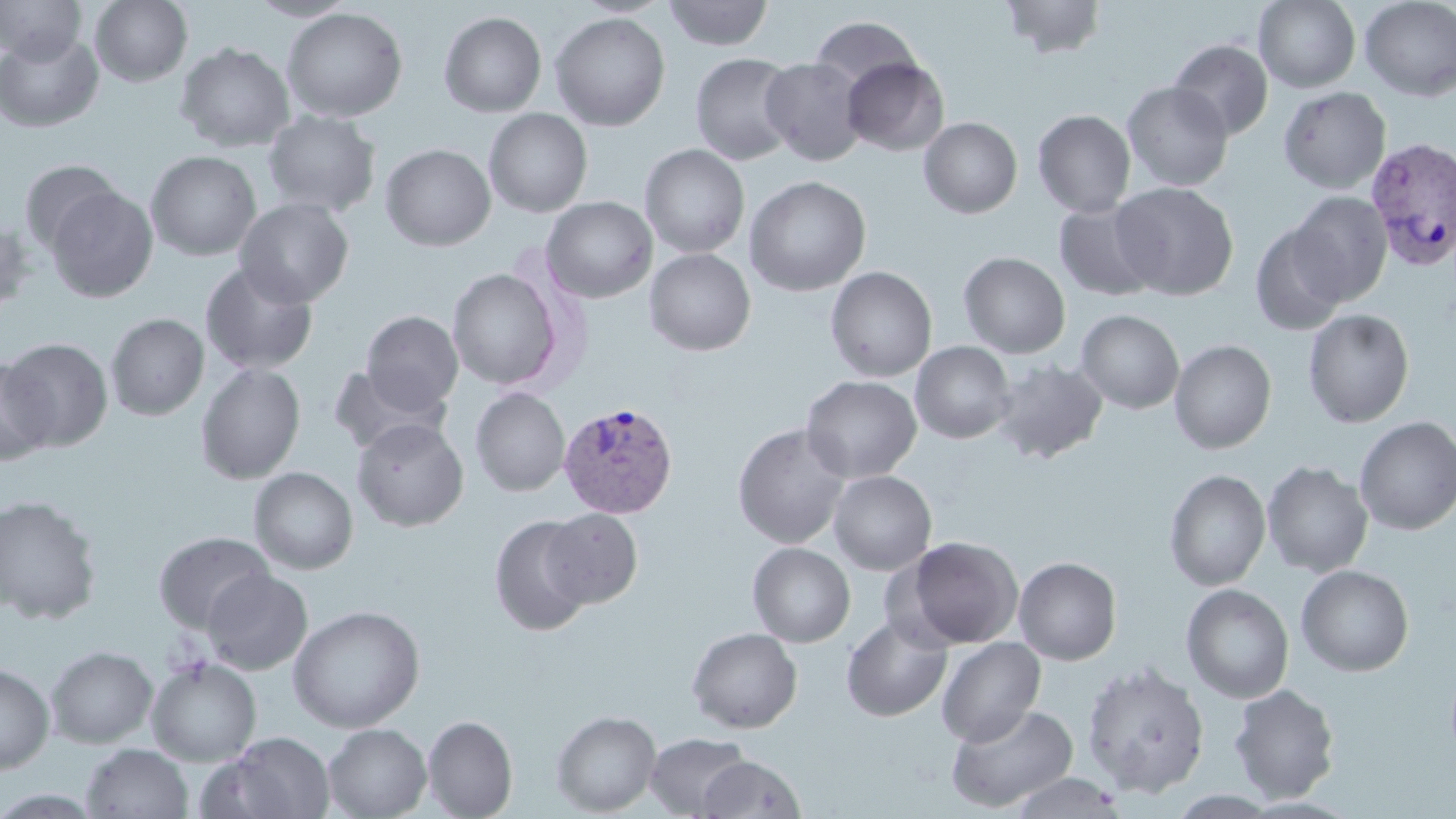
{
  "slide_level_diagnosis": "Plasmodium vivax",
  "preparation": "thin blood film",
  "magnification": "1000x",
  "image_size": "1456×819 pixels",
  "field_of_view": "one of a larger specimen",
  "modality": "light microscopy",
  "plasmodium_vivax_infected_red_blood_cell_locations": "approximate bounding boxes as (x1,y1)-(x2,y2) corner pairs in pixels: (1365,137)-(1455,272), (557,400)-(679,518)",
  "uninfected_red_blood_cell_locations": "approximate bounding boxes as (x1,y1)-(x2,y2) corner pairs in pixels: (1,0)-(87,64), (90,0)-(192,87), (246,0)-(359,21), (574,0)-(674,17), (663,0)-(774,50), (999,0)-(1109,60), (1254,0)-(1361,93), (1359,0)-(1456,101), (281,7)-(408,123), (438,11)-(547,117), (550,12)-(670,132), (809,16)-(921,96), (0,31)-(103,133), (1169,39)-(1273,140), (175,42)-(295,152), (690,52)-(799,165), (760,56)-(867,165), (842,57)-(949,156), (1122,81)-(1233,192), (1278,87)-(1391,193), (484,109)-(593,218), (1032,110)-(1136,218), (262,111)-(381,218), (919,117)-(1022,219), (380,144)-(496,251), (640,144)-(750,258), (145,150)-(262,261), (19,160)-(124,256), (744,176)-(871,297), (1111,182)-(1238,301), (46,186)-(158,303), (1288,191)-(1392,306), (541,197)-(657,303), (234,198)-(354,308), (1053,201)-(1162,301), (0,220)-(37,316), (1250,222)-(1350,336), (644,249)-(756,356), (958,251)-(1071,358), (200,261)-(319,375), (824,266)-(937,381), (447,268)-(564,390), (1302,308)-(1415,428), (1076,309)-(1184,414), (361,311)-(463,412), (106,313)-(209,420), (1,338)-(113,451), (1169,339)-(1277,454), (910,341)-(1016,444), (991,358)-(1108,465), (0,360)-(54,466), (195,362)-(306,484), (327,364)-(449,455), (800,375)-(921,482), (470,387)-(570,496), (1354,417)-(1456,535), (352,418)-(468,531), (733,423)-(851,549), (1261,460)-(1373,578), (248,467)-(358,574), (1164,469)-(1270,592), (828,470)-(937,575), (0,494)-(102,624), (542,508)-(642,608), (489,515)-(595,636), (153,531)-(273,633), (901,536)-(1024,649), (748,543)-(855,647), (1014,556)-(1122,665), (1296,564)-(1414,676), (202,568)-(313,675), (1181,583)-(1294,704), (288,604)-(425,733), (841,615)-(952,722), (687,627)-(803,733), (936,637)-(1046,747), (46,645)-(158,748), (146,656)-(262,766), (1082,661)-(1209,797), (0,663)-(55,774), (1228,683)-(1341,803), (946,702)-(1078,812), (551,710)-(662,816), (422,715)-(518,818), (323,723)-(431,819), (213,732)-(336,819), (645,732)-(752,817), (81,743)-(193,819), (697,754)-(807,818), (1006,771)-(1128,818), (1168,790)-(1280,818)",
  "stain": "May-Grünwald-Giemsa"
}